Find each cell and give its type.
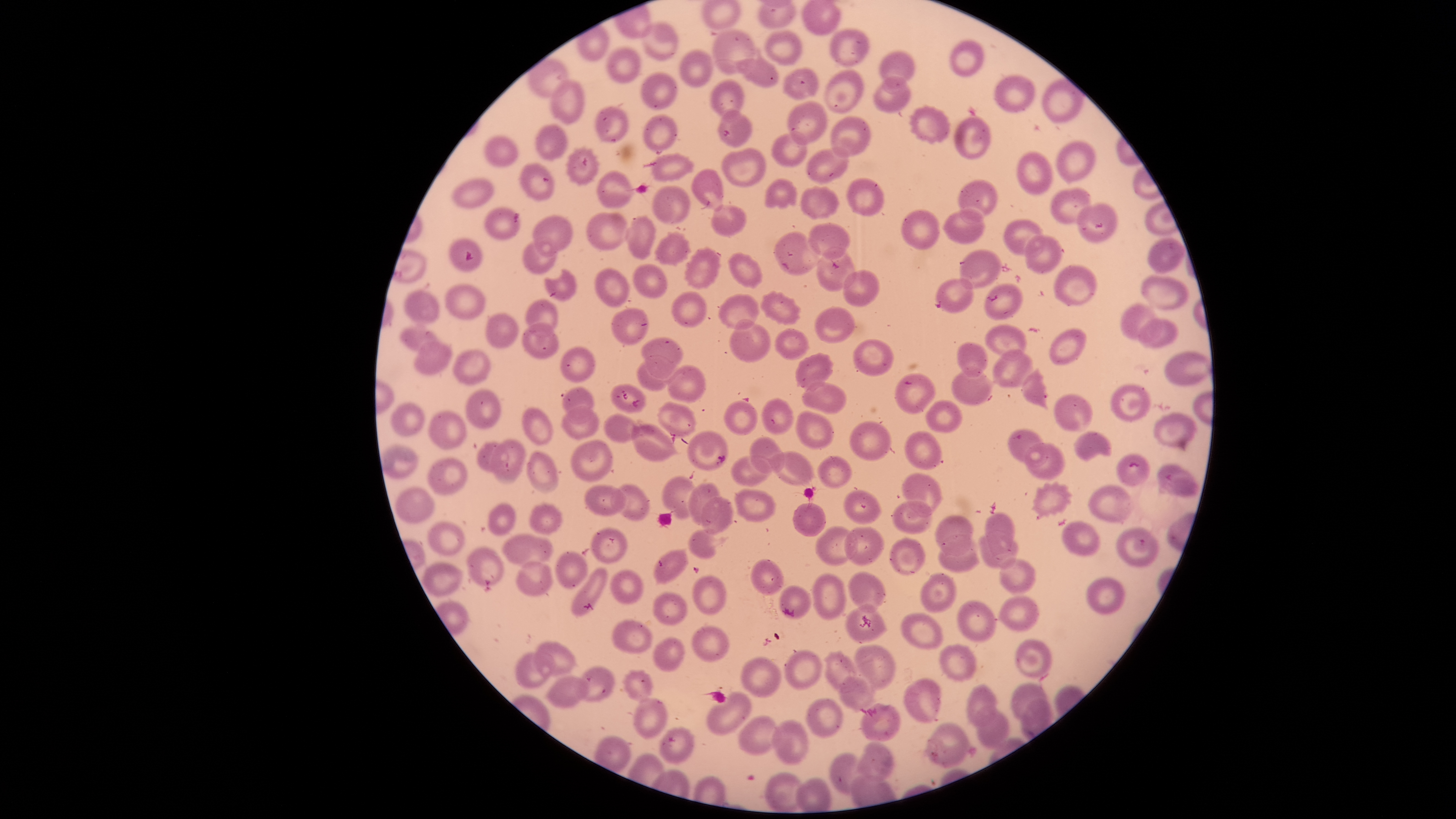

Approximate bounding boxes as {left, top, right, bottom} in pixels.
Parasitized red blood cells: {448, 240, 482, 272}, {1116, 454, 1149, 486}.
Uninfected red blood cells: {640, 21, 680, 61}, {711, 28, 759, 74}, {763, 28, 802, 67}, {827, 28, 870, 68}, {949, 40, 984, 77}, {605, 46, 641, 84}, {679, 48, 714, 88}, {878, 50, 916, 89}, {734, 55, 779, 88}, {782, 67, 819, 100}, {823, 69, 864, 114}, {641, 72, 678, 110}, {872, 74, 911, 113}, {995, 76, 1035, 112}, {549, 78, 584, 124}, {709, 79, 745, 118}, {786, 100, 828, 146}, {595, 104, 629, 142}, {909, 105, 951, 144}, {716, 109, 753, 147}, {644, 114, 678, 151}, {830, 116, 871, 158}, {954, 116, 991, 159}, {535, 122, 567, 161}, {771, 131, 808, 169}, {483, 135, 518, 167}, {1055, 140, 1096, 183}, {565, 145, 600, 187}, {805, 146, 850, 184}, {721, 148, 766, 188}, {1015, 150, 1054, 195}, {651, 152, 695, 182}, {518, 162, 554, 201}, {690, 169, 725, 211}, {596, 170, 635, 208}, {846, 177, 884, 217}, {451, 178, 494, 209}, {764, 178, 798, 210}, {957, 178, 999, 221}, {651, 185, 690, 225}, {800, 185, 840, 221}, {1050, 187, 1091, 224}, {1076, 202, 1116, 243}, {711, 203, 747, 238}, {483, 206, 521, 240}, {942, 207, 986, 245}, {900, 208, 940, 251}, {586, 212, 629, 251}, {532, 214, 574, 256}, {625, 215, 657, 259}, {1003, 219, 1046, 258}, {806, 222, 851, 260}, {653, 230, 693, 267}, {772, 231, 822, 276}, {1024, 233, 1065, 274}, {1147, 237, 1186, 274}, {522, 239, 558, 274}, {684, 246, 722, 290}, {816, 246, 857, 293}, {958, 249, 1003, 289}, {728, 251, 764, 289}, {633, 263, 668, 298}, {1053, 264, 1097, 305}, {594, 267, 630, 308}, {543, 268, 577, 301}, {842, 269, 880, 308}, {1140, 273, 1190, 311}, {934, 278, 974, 315}, {984, 282, 1024, 321}, {444, 283, 486, 320}, {403, 289, 440, 327}, {759, 290, 802, 326}, {671, 291, 708, 328}, {717, 292, 760, 330}, {525, 298, 557, 337}, {1119, 303, 1160, 342}, {814, 305, 856, 344}, {611, 307, 650, 346}, {485, 310, 519, 350}, {1137, 317, 1179, 349}, {729, 318, 771, 361}, {523, 321, 559, 360}, {983, 323, 1027, 361}, {399, 325, 448, 359}, {773, 328, 811, 361}, {1048, 329, 1086, 366}, {641, 337, 683, 380}, {852, 338, 894, 377}, {413, 340, 453, 375}, {956, 342, 988, 379}, {560, 347, 596, 383}, {452, 348, 492, 385}, {991, 348, 1034, 388}, {1163, 349, 1212, 386}, {795, 351, 835, 392}, {637, 354, 674, 391}, {667, 364, 706, 403}, {950, 365, 993, 406}, {1021, 367, 1048, 410}, {896, 374, 936, 413}, {800, 381, 847, 415}, {610, 383, 646, 413}, {1110, 383, 1151, 422}, {561, 386, 595, 424}, {464, 389, 502, 430}, {1053, 394, 1094, 432}, {760, 398, 795, 436}, {724, 400, 758, 436}, {389, 401, 425, 436}, {925, 401, 963, 433}, {657, 402, 697, 438}, {522, 405, 554, 445}, {560, 405, 600, 440}, {795, 409, 835, 450}, {427, 410, 467, 449}, {1153, 411, 1198, 452}, {602, 412, 647, 444}, {848, 420, 893, 463}, {630, 424, 678, 463}, {1007, 429, 1049, 468}, {687, 431, 729, 472}, {1072, 431, 1112, 462}, {906, 432, 941, 468}, {749, 436, 785, 475}, {489, 438, 525, 485}, {570, 439, 612, 483}, {1023, 440, 1066, 480}, {476, 441, 506, 472}, {381, 444, 420, 479}, {525, 450, 559, 496}, {768, 451, 815, 487}, {730, 455, 774, 488}, {427, 456, 469, 497}, {817, 456, 852, 489}, {1157, 463, 1199, 498}, {901, 472, 941, 517}, {662, 475, 701, 520}, {686, 481, 723, 526}, {1030, 481, 1074, 520}, {614, 483, 650, 521}, {584, 484, 626, 517}, {1087, 484, 1133, 524}, {394, 485, 436, 524}, {733, 488, 777, 523}, {843, 488, 882, 525}, {700, 495, 734, 535}, {891, 499, 933, 534}, {487, 502, 516, 537}, {529, 502, 562, 535}, {792, 502, 827, 537}, {984, 512, 1015, 555}, {934, 515, 975, 558}, {427, 520, 466, 556}, {1061, 521, 1102, 557}, {814, 525, 859, 567}, {590, 526, 628, 564}, {843, 526, 883, 566}, {1114, 526, 1159, 567}, {687, 527, 729, 559}, {502, 531, 554, 568}, {937, 532, 981, 573}, {977, 532, 1019, 569}, {888, 537, 925, 577}, {466, 545, 504, 588}, {652, 547, 689, 586}, {555, 551, 588, 588}, {998, 557, 1038, 594}, {749, 558, 784, 597}, {514, 561, 554, 597}, {422, 562, 464, 598}, {571, 568, 609, 618}, {609, 569, 644, 605}, {847, 571, 887, 614}, {921, 571, 957, 614}, {812, 572, 847, 621}, {692, 575, 727, 615}, {1085, 576, 1125, 615}, {778, 584, 811, 620}, {652, 592, 689, 626}, {996, 595, 1039, 632}, {956, 600, 997, 642}, {845, 603, 889, 642}, {900, 612, 943, 649}, {611, 619, 654, 655}, {691, 626, 731, 662}, {653, 636, 686, 672}, {1015, 639, 1052, 679}, {531, 640, 578, 679}, {938, 642, 978, 683}, {853, 644, 896, 692}, {783, 649, 822, 690}, {822, 649, 861, 694}, {515, 651, 552, 690}, {740, 656, 782, 698}, {574, 665, 616, 703}, {621, 669, 654, 702}, {545, 675, 590, 709}, {839, 675, 877, 713}, {902, 677, 941, 723}, {1010, 681, 1048, 724}, {967, 683, 996, 727}, {706, 691, 752, 736}, {632, 696, 668, 740}, {806, 697, 843, 737}, {860, 703, 901, 743}, {975, 707, 1010, 749}, {737, 715, 779, 755}, {770, 718, 809, 766}, {922, 721, 975, 769}, {657, 726, 696, 765}, {854, 742, 894, 782}, {829, 752, 870, 794}, {764, 772, 807, 811}.
No white blood cells identified.

{
  "field_of_view": "single",
  "species": "Plasmodium falciparum",
  "visible_region": "circular",
  "image_size": "1456×819 pixels",
  "capture": "smartphone photograph through the microscope eyepiece",
  "preparation": "thin blood film",
  "stain": "Giemsa"
}